State which cell type is depicted.
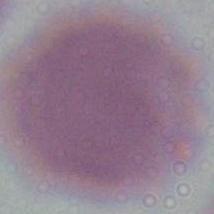

An erythrocyte.

Photomicrograph. Captured at 1000x magnification.